Describe the morphology of the erythrocytes.
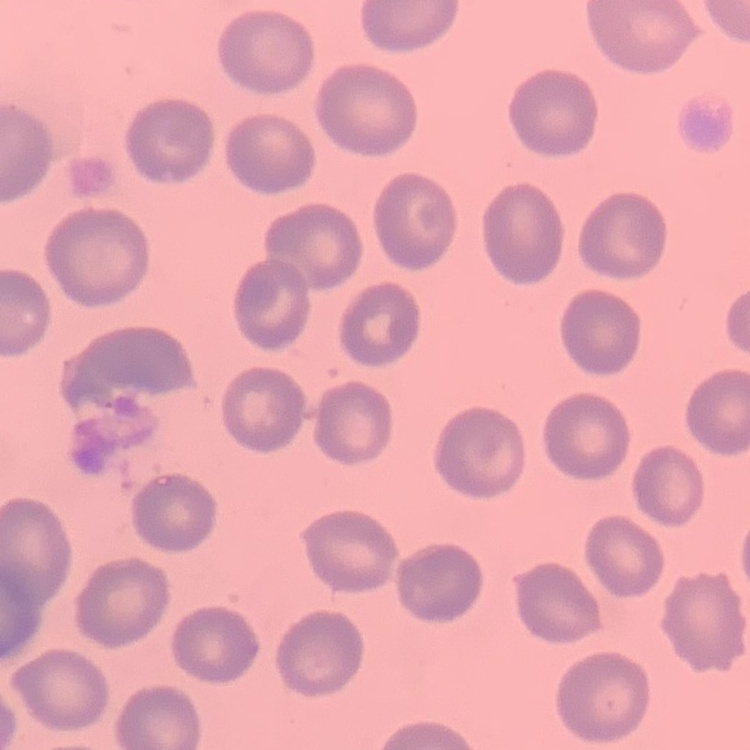

They show no rouleaux formation.

image type = square crop of a larger photomicrograph
preparation = thin blood film
stain = Field's or Giemsa